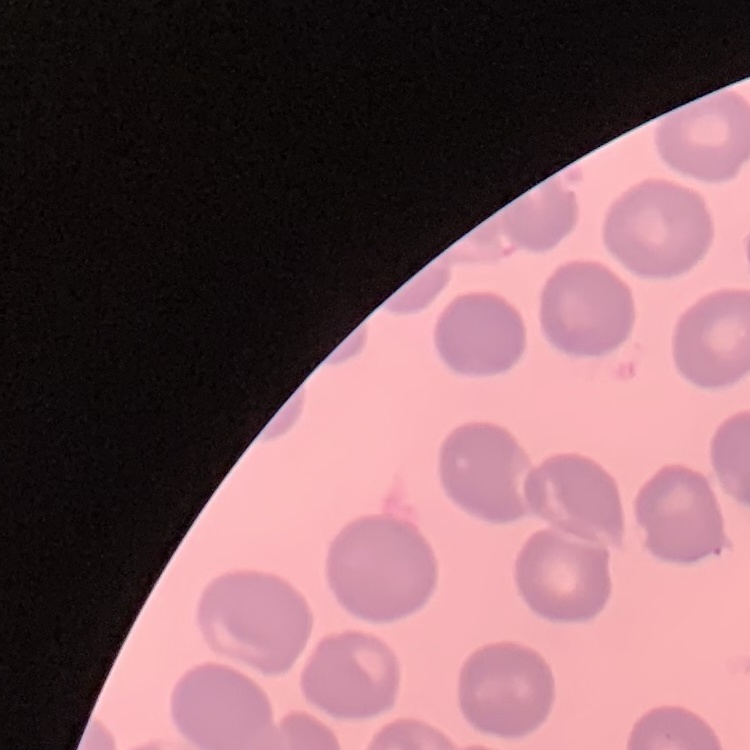
Summary:
  - Erythrocyte morphology: no rouleaux formation
  - Image type: one tile cut from a larger photomicrograph
  - Preparation: thin blood film
  - Stain: Field's or Giemsa